Assess for Plasmodium parasites.
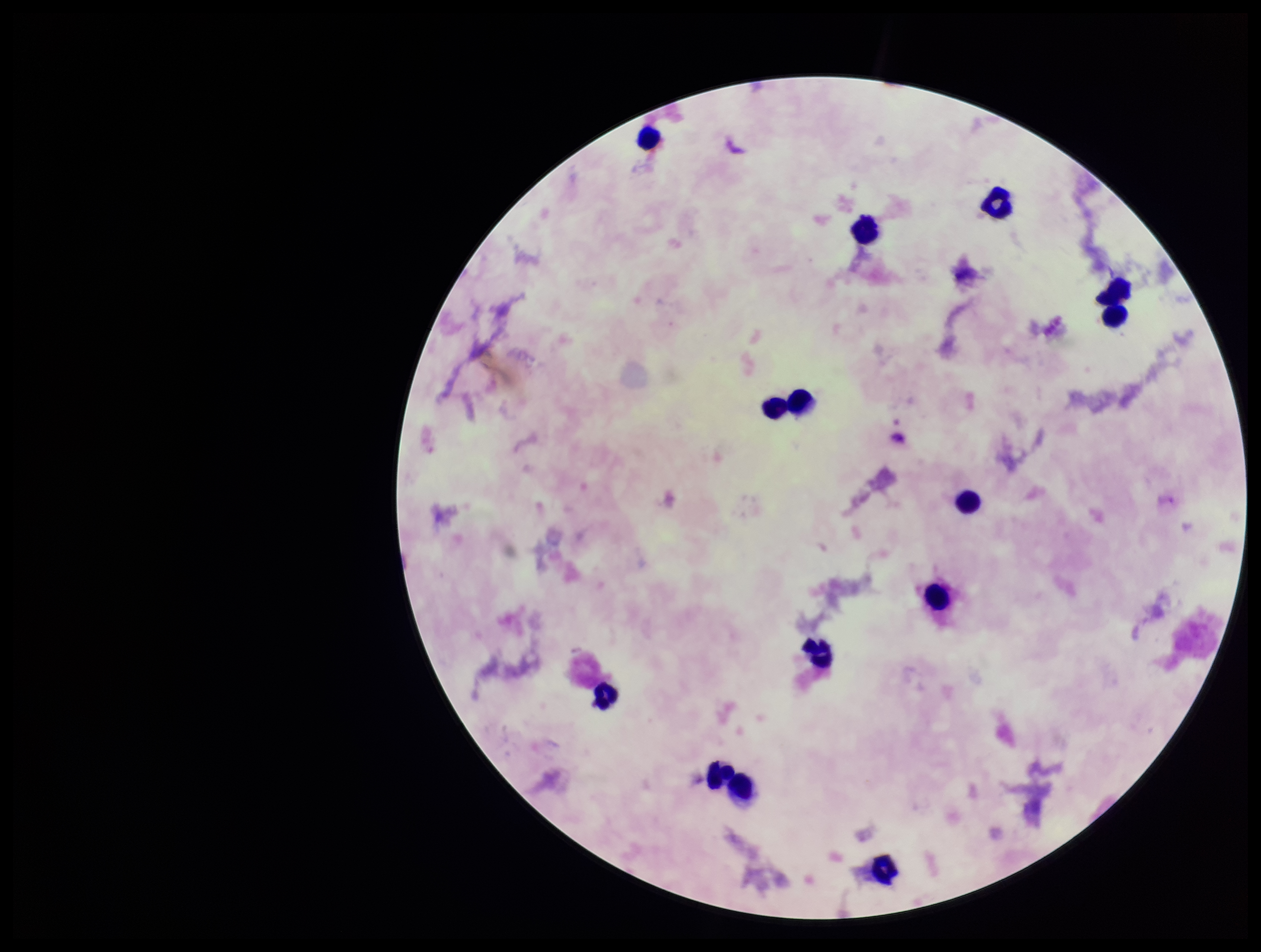

None identified.

Summary:
  - Species reported for this patient: Plasmodium vivax
  - Leukocyte count: 14
  - Patient malaria status: positive
  - Image size: 1261×952 pixels
  - Parasite count: 0
  - Stain: Giemsa
  - Preparation: thick
  - Field of view: single
  - Capture: smartphone photograph through the microscope eyepiece